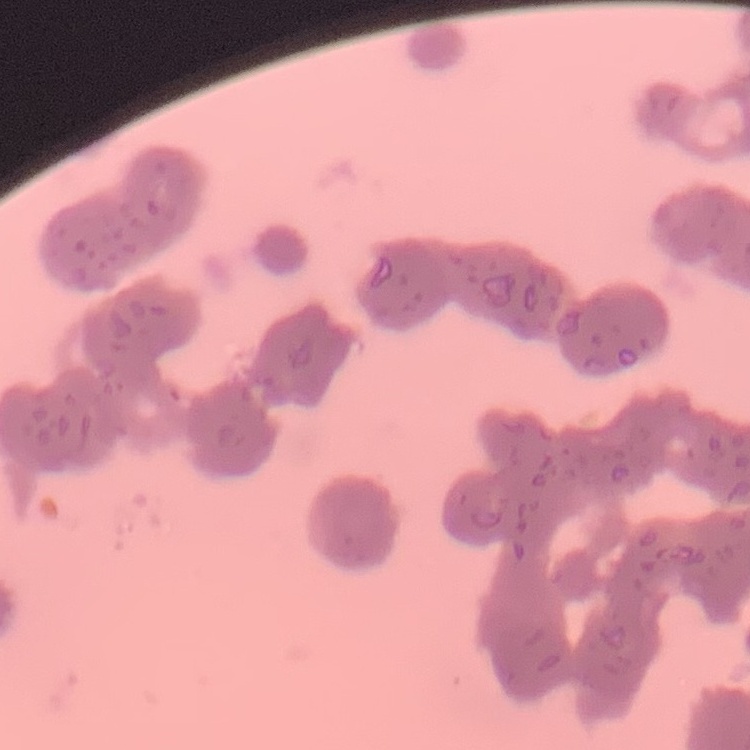

red blood cell morphology = rouleaux formation
image type = square crop of a larger photomicrograph
preparation = thin blood film
stain = Field's or Giemsa